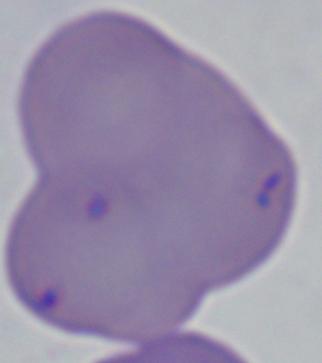
1000x magnification. A Babesia parasite is seen. Photomicrograph.